Locate every blood parasite and identify its species.
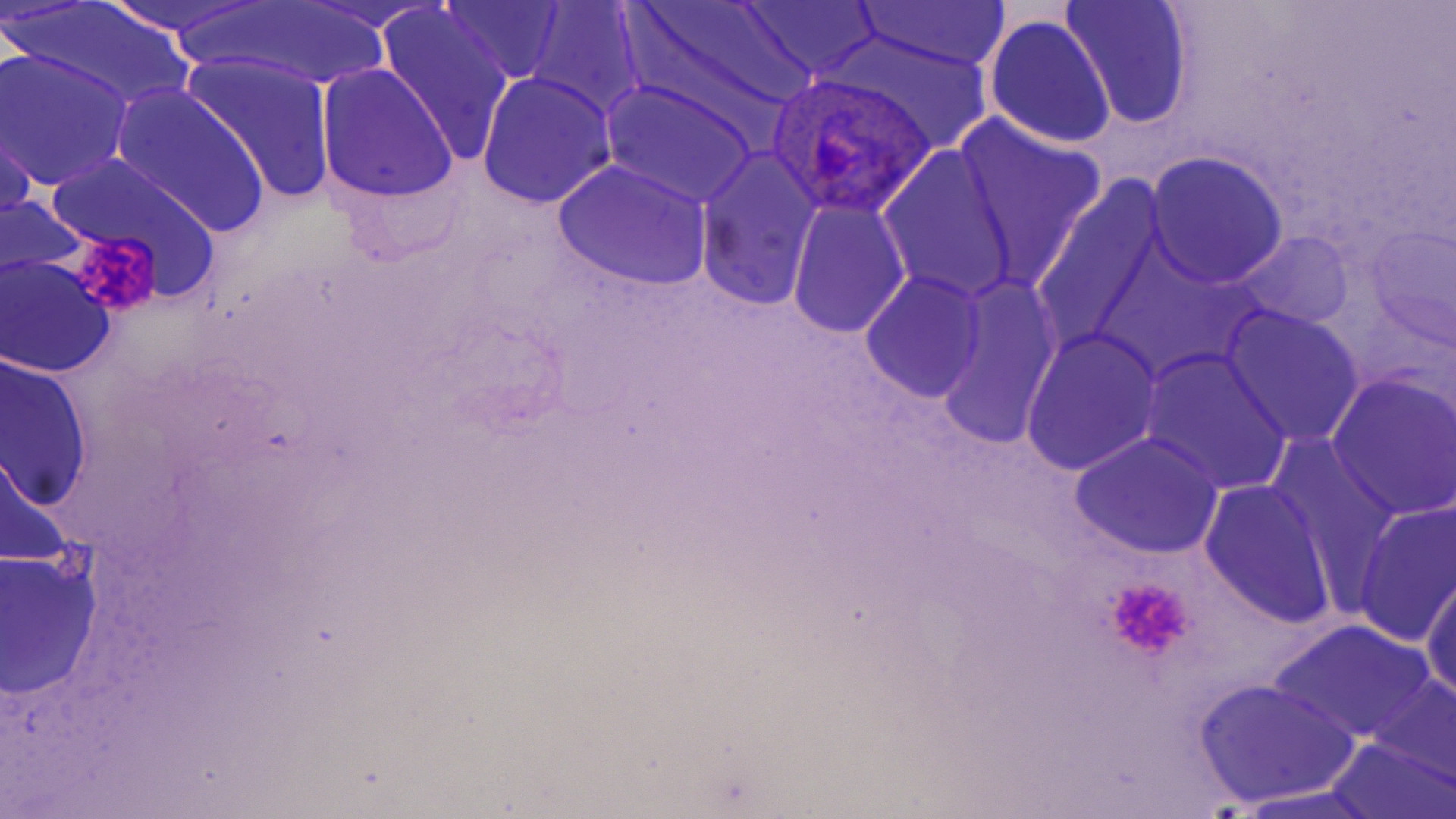
Approximate bounding boxes as (x1,y1)-(x2,y2) corner pairs in pixels.
Plasmodium ovale-infected red blood cells: (761,74)-(941,220).
No Plasmodium falciparum, Plasmodium malariae, Plasmodium vivax, Babesia divergens, or Trypanosoma brucei observed.

slide-level diagnosis = Plasmodium ovale
image size = 1456×819 pixels
magnification = 1000x
stain = May-Grünwald-Giemsa
uninfected red blood cell locations = approximate bounding boxes as (x1,y1)-(x2,y2) corner pairs in pixels: (95,0)-(259,38), (300,0)-(446,33), (171,1)-(396,95), (438,1)-(568,86), (626,1)-(814,119), (736,1)-(887,82), (1060,1)-(1196,130), (849,2)-(1012,73), (10,4)-(194,114), (524,4)-(647,119), (375,5)-(516,165), (983,15)-(1117,150), (819,30)-(992,152), (0,50)-(133,190), (181,52)-(338,207), (315,65)-(460,203), (478,72)-(618,208), (600,79)-(761,207), (111,85)-(273,238), (0,107)-(37,235), (951,116)-(1107,286), (695,148)-(824,310), (880,148)-(1017,304), (44,150)-(230,299), (1142,151)-(1289,289), (554,160)-(712,291), (1029,184)-(1171,359), (0,195)-(91,289), (787,202)-(910,338), (1361,221)-(1454,348), (1233,227)-(1355,336), (0,256)-(117,379), (860,273)-(989,405), (932,275)-(1064,449), (1219,305)-(1364,447), (1021,327)-(1163,477), (1138,349)-(1292,496), (1,355)-(92,516), (1326,373)-(1456,520), (1069,433)-(1224,560), (0,449)-(81,577), (1199,479)-(1339,632), (1352,500)-(1456,648), (0,547)-(105,700), (1421,566)-(1456,711), (1269,619)-(1435,744), (1359,671)-(1456,794), (1194,678)-(1361,809), (1325,733)-(1454,819), (1229,788)-(1388,818)
preparation = thin blood film
field of view = one of a larger specimen
modality = light microscopy
platelet locations = approximate bounding boxes as (x1,y1)-(x2,y2) corner pairs in pixels: (65,227)-(168,320), (1101,573)-(1196,666)